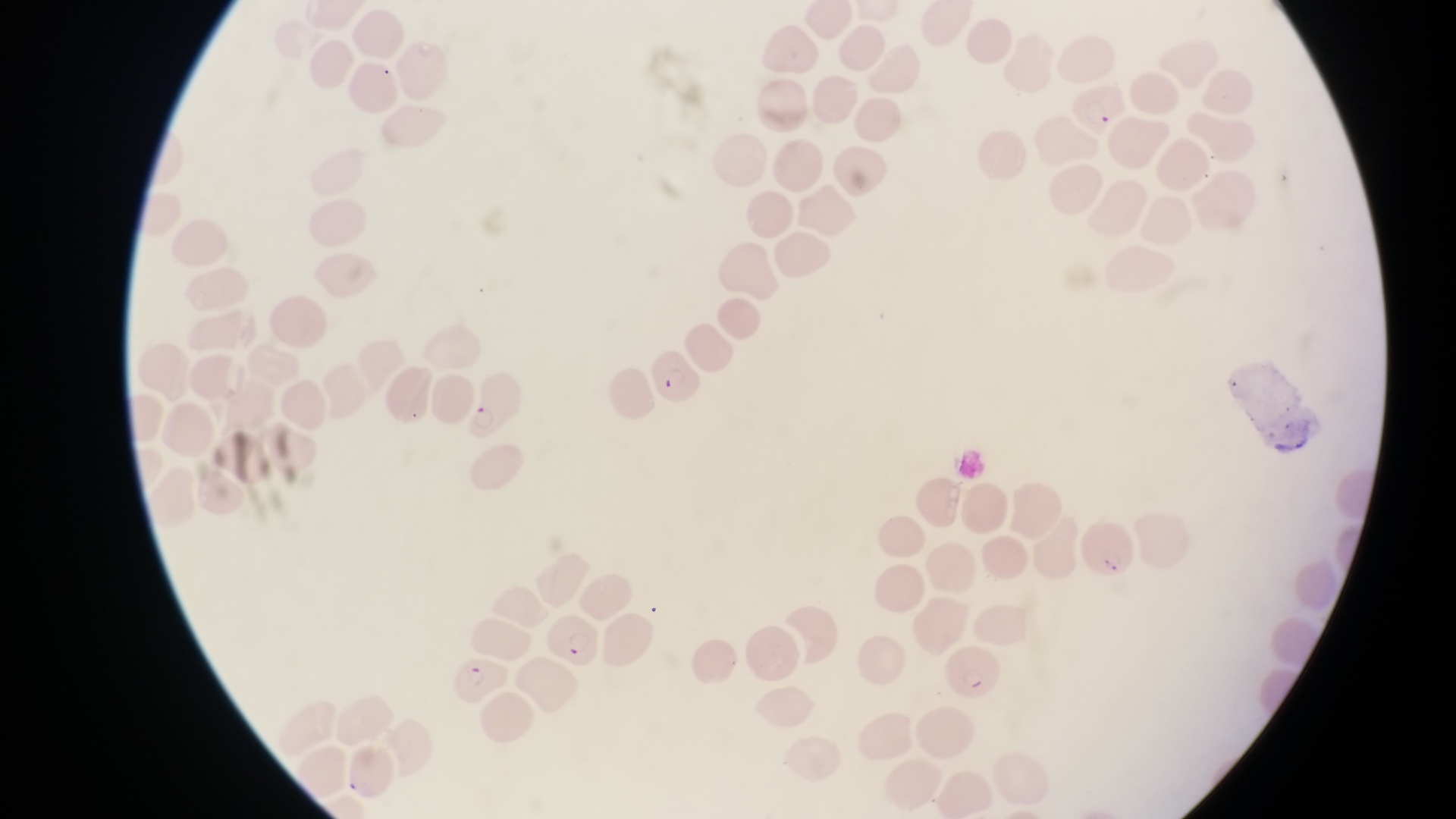

Approximate bounding boxes as (left, top, right, bottom) in pixels.
Summary:
  - Parasitised red blood cell locations: (1070, 86, 1136, 139), (647, 349, 706, 412), (468, 372, 528, 445), (1078, 518, 1144, 592), (944, 642, 1000, 706), (449, 657, 509, 713)
  - Capture: smartphone photograph through the eyepiece of an Olympus CX-23 microscope
  - Country: Uganda
  - Preparation: thin blood film
  - Image size: 1456×819 pixels
  - Field of view: single
  - Magnification: 1000x